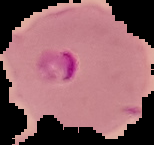

Summary:
  - Preparation: thin blood film
  - Image type: segmented cell region with the area outside set to black
  - Image size: 154×145 pixels
  - Result: Plasmodium parasites identified